Identify the parasite.
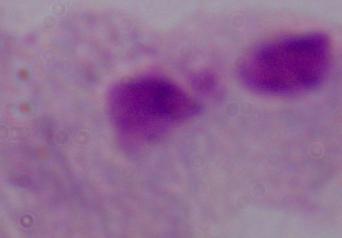
This is a trichomonad.

Summary:
  - Magnification: 1000x
  - Modality: micrograph